Assess this cell for malaria.
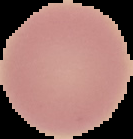

It is uninfected.

Segmented cell region on a black background. Image is 133×139 pixels. From a thin blood smear.